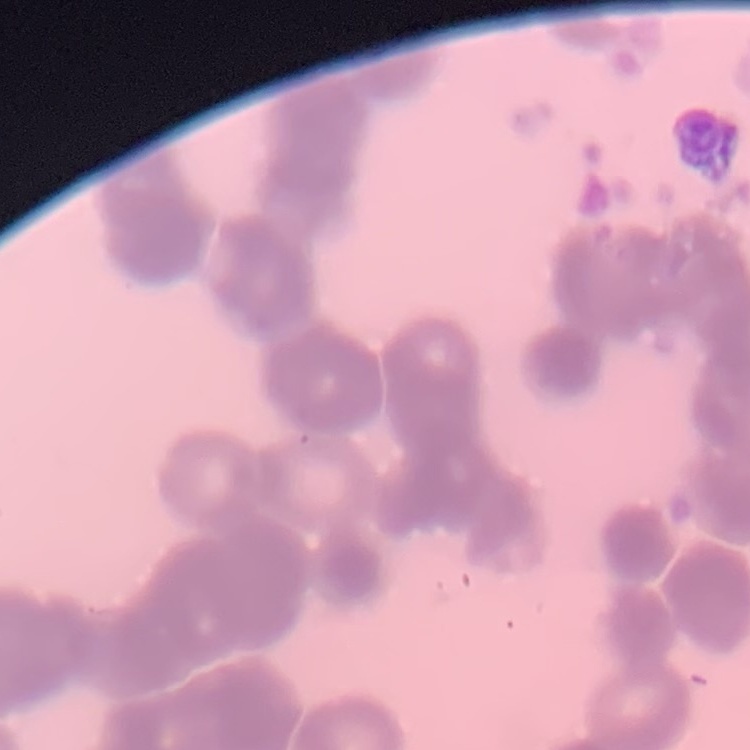
erythrocyte morphology = rouleaux formation
stain = Field's or Giemsa
preparation = thin blood smear
image type = one tile cut from a larger photomicrograph